State which parasite is depicted.
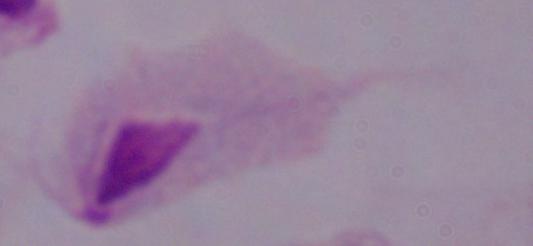
A trichomonad.

Micrograph. Captured at 1000x magnification.